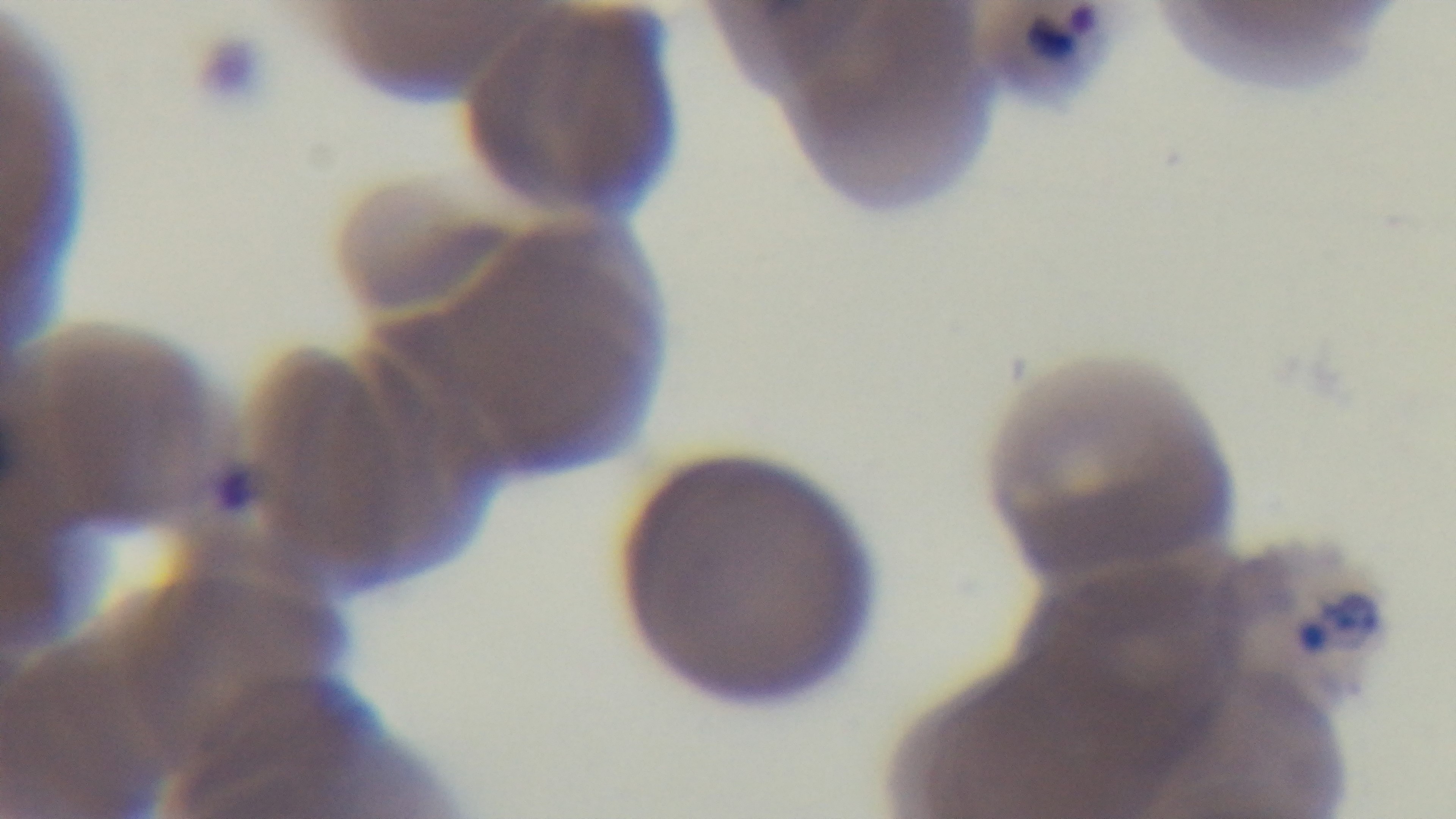
{
  "stain": "Giemsa",
  "field_of_view": "single",
  "modality": "light microscopy",
  "capture": "mounted 4K digital camera",
  "objective": "100x oil immersion",
  "preparation": "thin blood film",
  "malaria_status": "positive"
}